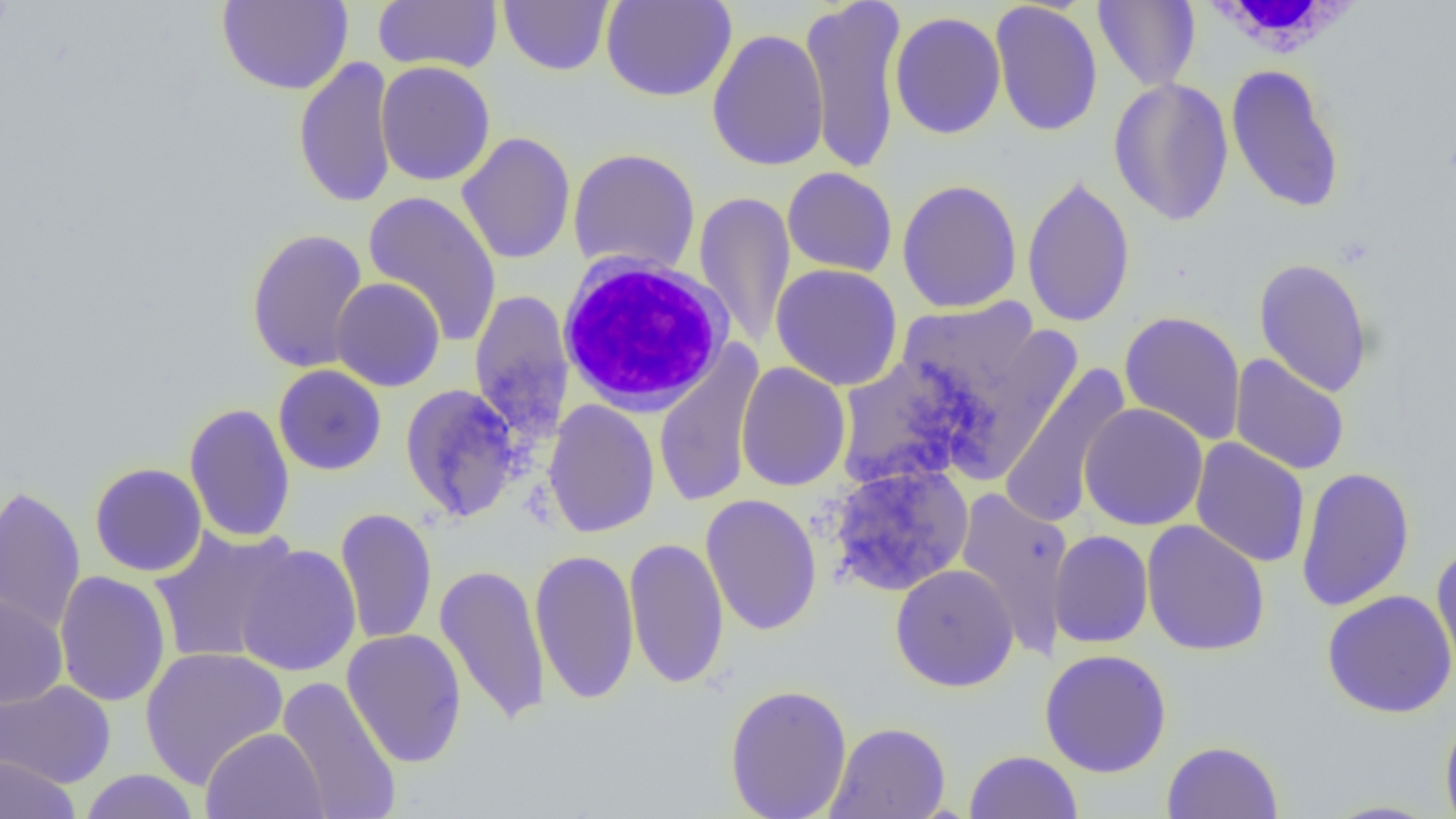
slide_level_diagnosis: no evidence of blood parasites
uninfected_red_blood_cell_locations: 'approximate bounding boxes as (x1, y1, x2, y2) in pixels: (216, 0, 354, 95), (498, 0, 614, 76), (601, 0, 737, 102), (799, 0, 907, 175), (1093, 0, 1200, 91), (373, 1, 503, 74), (989, 1, 1104, 137), (889, 11, 1007, 140), (706, 29, 830, 172), (293, 55, 398, 210), (375, 61, 496, 186), (1225, 63, 1345, 214), (1108, 77, 1234, 226), (457, 132, 576, 265), (568, 148, 701, 278), (782, 167, 898, 277), (1021, 175, 1136, 328), (896, 179, 1023, 314), (363, 190, 503, 348), (694, 191, 796, 349), (246, 228, 369, 373), (1253, 258, 1374, 397), (770, 263, 903, 391), (331, 278, 445, 392), (469, 290, 575, 442), (897, 299, 1042, 408), (1119, 310, 1246, 446), (945, 320, 1082, 483), (653, 342, 765, 510), (835, 354, 989, 490), (1229, 354, 1350, 475), (735, 362, 851, 492), (997, 363, 1132, 529), (273, 365, 387, 476), (399, 383, 524, 523), (543, 399, 660, 539), (183, 402, 296, 544), (1079, 402, 1209, 531), (1190, 438, 1310, 568), (89, 462, 207, 577), (827, 463, 974, 597), (1295, 466, 1415, 613), (0, 484, 86, 636), (955, 487, 1075, 659), (700, 494, 822, 636), (334, 506, 437, 646), (1141, 520, 1270, 657), (150, 526, 301, 665), (1048, 530, 1153, 648), (623, 536, 729, 689), (234, 543, 362, 677), (1431, 544, 1456, 686), (530, 549, 640, 705), (435, 563, 551, 727), (890, 563, 1019, 692), (54, 571, 172, 707), (1322, 590, 1456, 718), (0, 592, 68, 708), (341, 628, 467, 768), (139, 646, 289, 787), (1040, 649, 1172, 778), (276, 676, 402, 819), (0, 679, 116, 788), (724, 683, 852, 819), (1440, 705, 1456, 819), (825, 721, 951, 819), (200, 727, 329, 819), (1162, 740, 1284, 818), (964, 750, 1083, 819), (1, 755, 80, 819), (78, 769, 201, 819)'
field_of_view: one of a larger specimen
magnification: 1000x
preparation: thin blood smear
image_size: 1456×819 pixels
modality: light microscopy
white_blood_cell_locations: 'approximate bounding boxes as (x1, y1, x2, y2) in pixels: (1193, 0, 1368, 59), (554, 253, 734, 417)'